Point out each Plasmodium parasite.
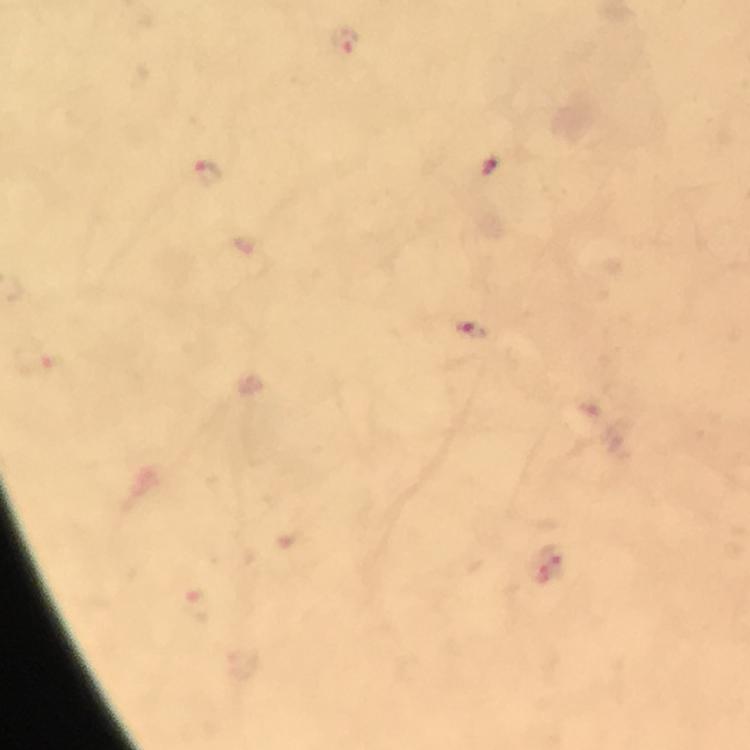
Approximate centers as {x, y} in pixels.
Plasmodium parasites: {344, 41}, {489, 167}, {207, 174}, {472, 331}, {551, 560}.

Summary:
  - Preparation: thick blood film
  - Context: from a diagnostic examination for malaria
  - Immersion oil: used
  - Stain: Giemsa
  - Cropped from: one field of view
  - Capture: smartphone photograph through a microscope
  - Magnification: 100x
  - Image size: 750×750 pixels